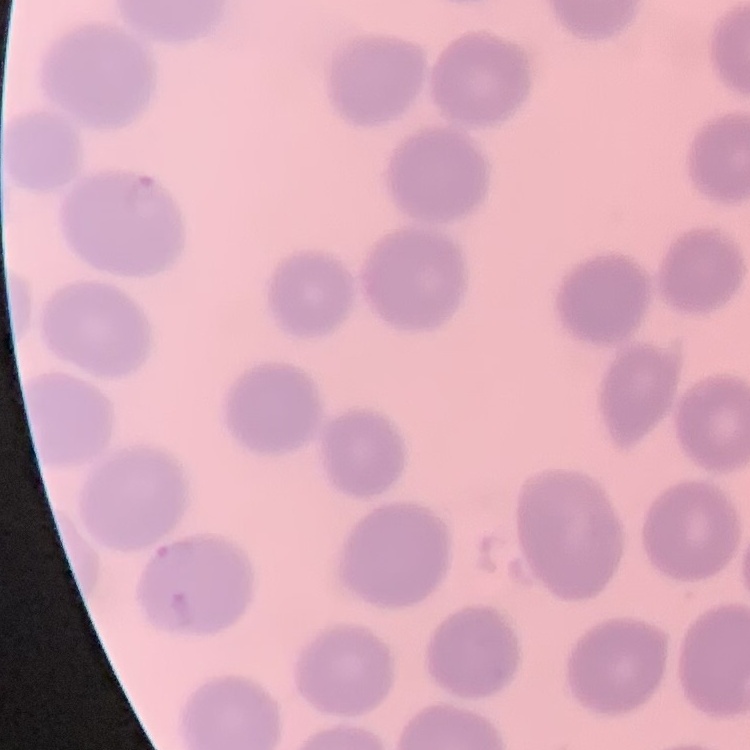

The red blood cells exhibit no rouleaux formation. Thin peripheral smear. Square crop of a larger photomicrograph. Field's or Giemsa stain.